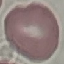 Result: negative for malaria parasites. Giemsa stain. Photographed with a smartphone camera at the microscope eyepiece. Thin blood film. Automatically extracted cell patch, resized to 64 × 64 pixels.